Assess the morphology of the erythrocytes.
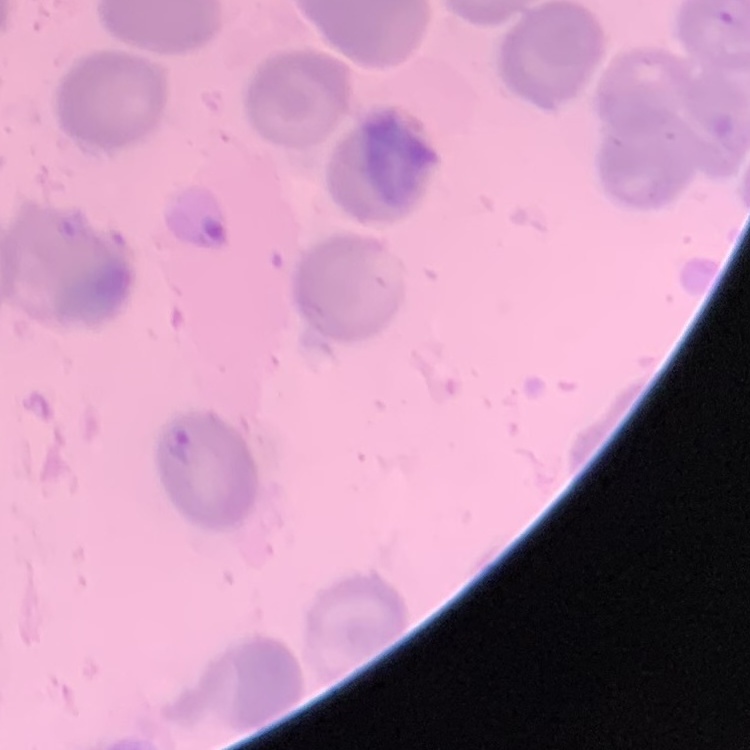

They show no rouleaux formation.

image type = one tile cut from a larger photomicrograph
stain = Field's or Giemsa
preparation = thin blood smear